Give the position of every Plasmodium parasite.
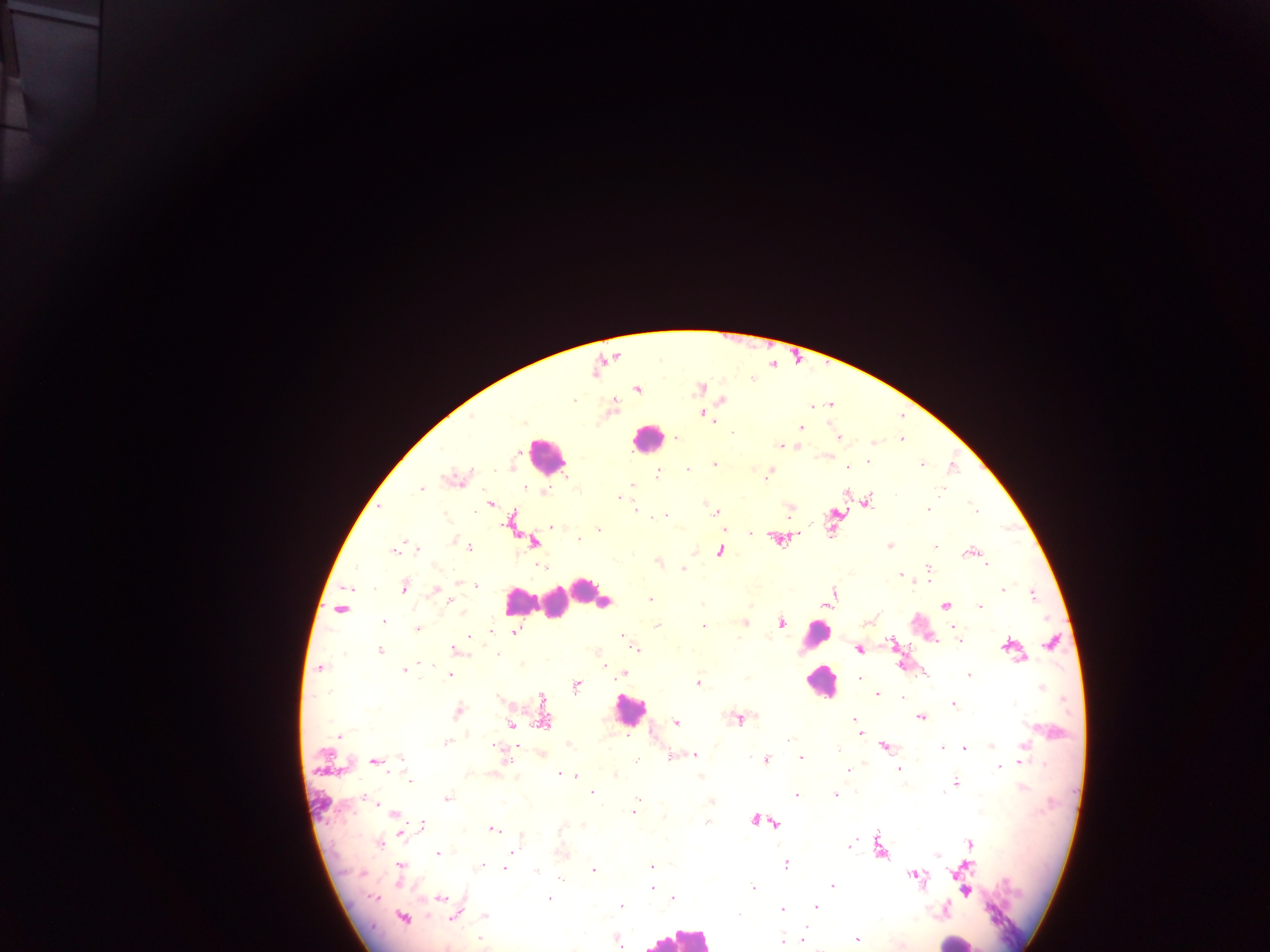

Approximate centers as [x, y] in pixels.
Plasmodium parasites: [700, 388], [637, 389], [723, 400], [703, 414], [712, 421], [801, 428], [733, 434], [677, 437], [839, 438], [902, 438], [873, 442], [780, 445], [796, 445], [868, 462], [714, 464], [922, 465], [847, 468], [687, 469], [658, 474], [769, 475], [454, 479], [633, 485], [421, 490], [941, 491], [544, 492], [619, 497], [868, 502], [490, 503], [708, 506], [636, 509], [928, 509], [790, 510], [974, 510], [716, 512], [659, 516], [663, 516], [513, 519], [551, 527], [598, 530], [751, 533], [580, 539], [776, 539], [455, 542], [535, 542], [461, 543], [466, 546], [889, 546], [935, 546], [416, 547], [394, 549], [720, 551], [969, 552], [659, 562], [987, 564], [541, 566], [928, 567], [683, 569], [900, 574], [915, 582], [929, 582], [476, 585], [404, 587], [1003, 589], [436, 591], [834, 592], [1032, 595], [651, 600], [450, 601], [826, 605], [946, 605], [979, 606], [340, 609], [384, 621], [745, 622], [781, 623], [656, 626], [703, 626], [953, 627], [417, 628], [490, 632], [515, 632], [622, 636], [469, 638], [958, 640], [890, 641], [1051, 642], [1008, 646], [635, 649], [858, 649], [380, 650], [457, 650], [497, 654], [900, 665], [320, 668], [404, 670], [623, 673], [450, 674], [926, 674], [969, 676], [860, 680], [698, 683], [577, 686], [1041, 688], [877, 694], [902, 697], [499, 699], [1014, 703], [953, 704], [458, 712], [853, 718], [920, 718], [738, 719], [543, 720], [675, 722], [510, 724], [860, 733], [338, 736], [787, 740], [448, 742], [884, 746], [992, 746], [1025, 746], [942, 748], [965, 748], [837, 749], [542, 753], [695, 755], [504, 756], [672, 757], [800, 759], [765, 760], [402, 761], [374, 762], [1022, 763], [899, 768], [999, 768], [848, 770], [561, 775], [571, 775], [615, 775], [408, 777], [955, 782], [592, 792], [796, 795], [835, 795], [447, 798], [371, 801], [711, 801], [637, 803], [634, 811], [394, 813], [755, 820], [707, 822], [423, 824], [493, 829], [562, 829], [401, 831], [379, 843], [970, 843], [850, 846], [880, 847], [563, 852], [438, 854], [512, 854], [936, 855], [482, 865], [786, 865], [652, 866], [966, 866], [505, 867], [594, 870], [400, 871], [536, 872], [915, 875], [560, 878], [652, 886], [832, 886], [753, 888], [967, 892], [374, 896], [441, 898], [674, 898], [549, 899], [621, 906], [816, 906], [782, 910], [455, 914], [738, 914], [485, 915], [403, 919], [806, 929], [857, 938], [803, 939], [617, 940], [481, 941], [782, 942].

Leukocyte locations: [646, 438], [545, 455], [587, 594], [520, 600], [554, 603], [815, 637], [820, 682], [629, 711], [677, 937], [954, 941]. Collected in Ghana. Thick blood film. One field of view. Image is 1270×952 pixels. Mobile-phone photograph taken through the microscope.